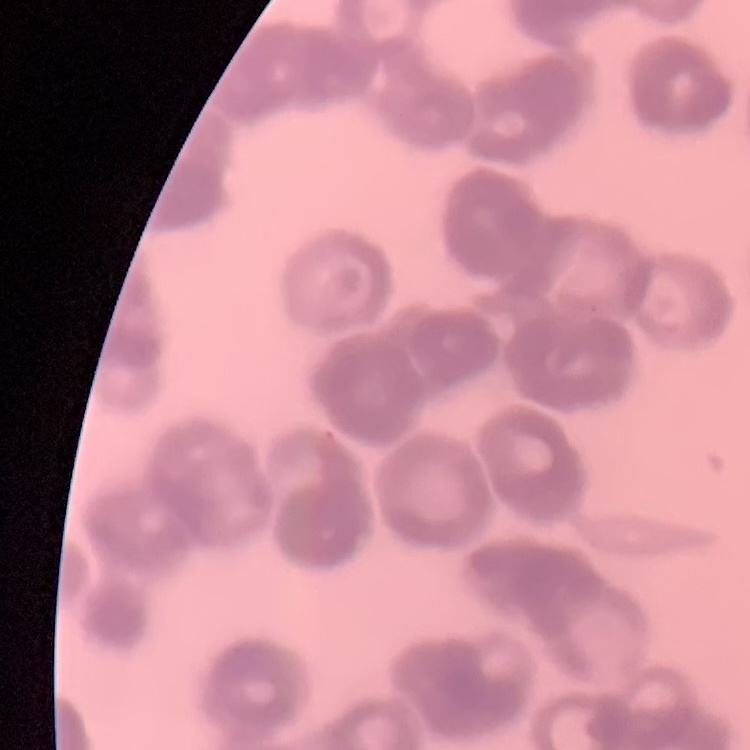 The red blood cells exhibit rouleaux formation. Field's or Giemsa stain. Thin peripheral smear. Square crop of a larger photomicrograph.